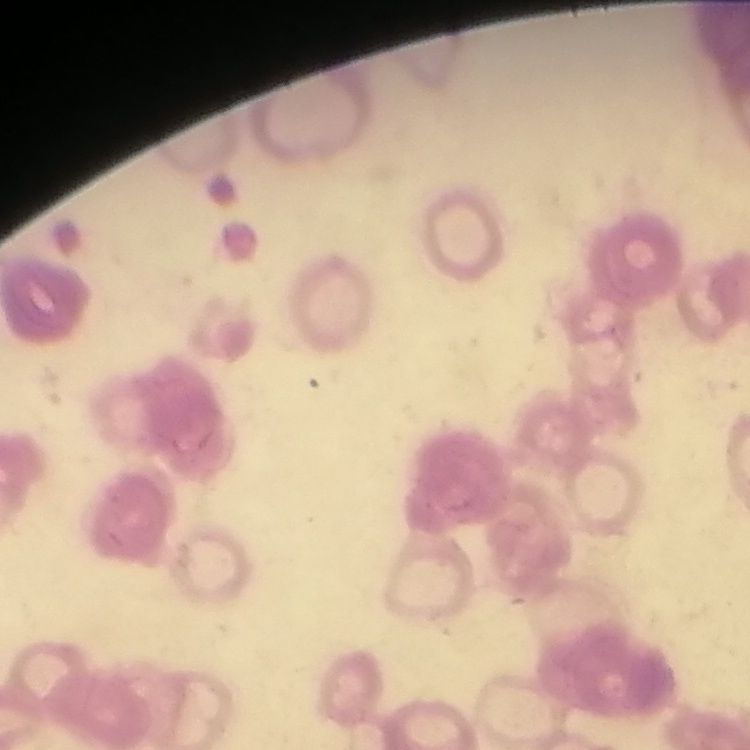
{
  "erythrocyte_morphology": "rouleaux formation",
  "stain": "Field's or Giemsa",
  "preparation": "thin blood film",
  "image_type": "square crop of a larger photomicrograph"
}